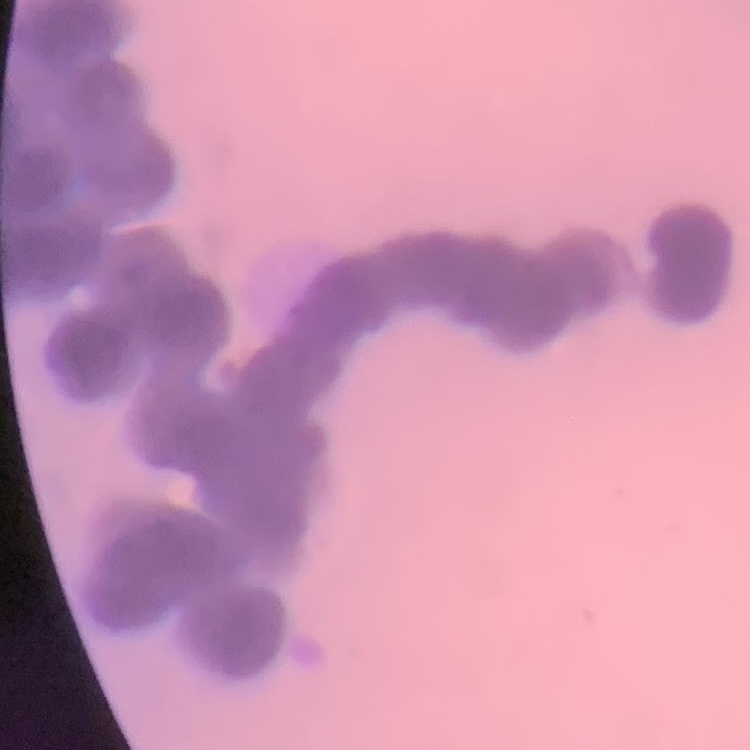

Summary:
  - Erythrocyte morphology: rouleaux formation
  - Image type: one tile cut from a larger photomicrograph
  - Preparation: thin blood smear
  - Stain: Field's or Giemsa